Identify the parasite.
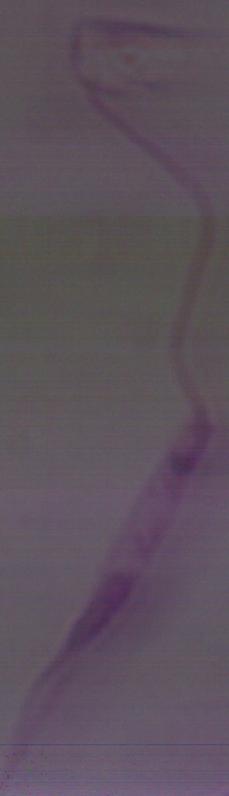
Leishmania.

Summary:
  - Magnification: 1000x
  - Modality: photomicrograph